Point out leukocytes.
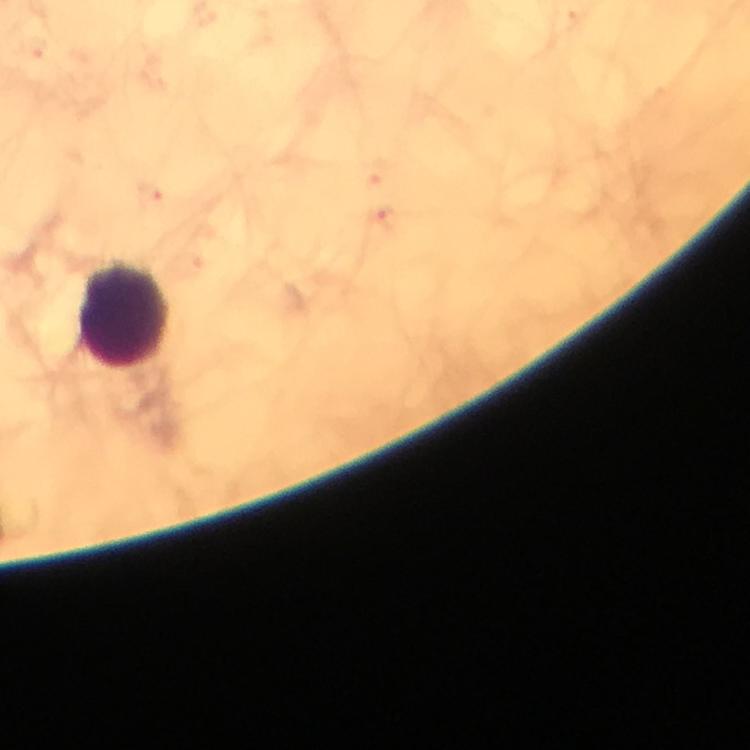

Approximate centers as {x, y} in pixels.
Leukocytes: {125, 315}.

preparation = thick blood smear
immersion oil = used
magnification = 100x
stain = Giemsa
capture = smartphone camera through the microscope
Plasmodium parasites = none seen
cropped from = a single field of view
image size = 750×750 pixels
context = from a malaria diagnostic workup